Classify this cell by malaria status.
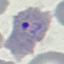

Parasitized.

Giemsa stain. Thin blood film. Photographed with a smartphone camera at the microscope eyepiece. Cell patch, automatically extracted from a larger field of view and resized to 64 × 64 pixels.